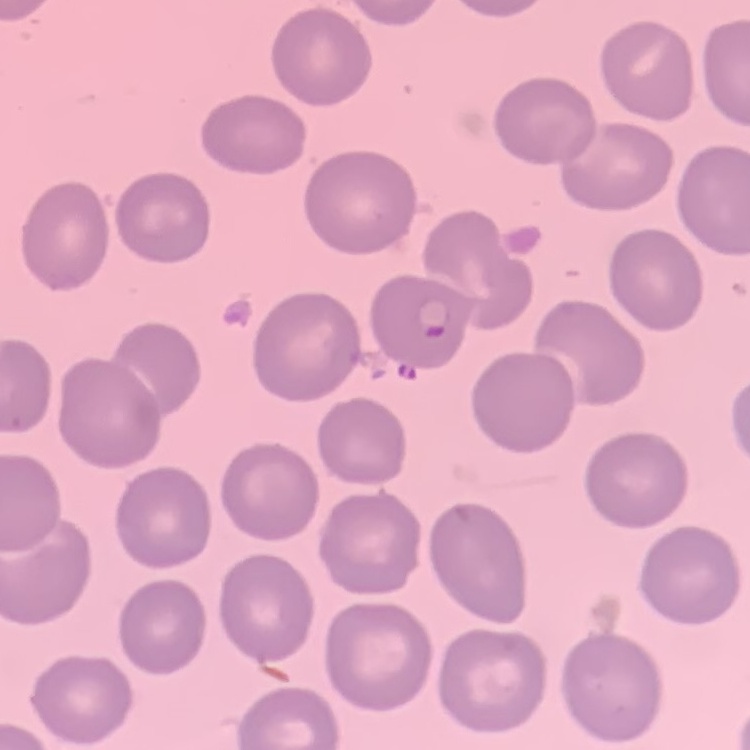
The red blood cells exhibit no rouleaux formation. Field's or Giemsa stain. Square crop of a larger photomicrograph. Thin blood film.